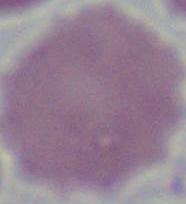
magnification = 1000x
identification = erythrocyte
modality = photomicrograph